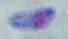
Summary:
  - Identification: Toxoplasma gondii
  - Magnification: 1000x
  - Modality: photomicrograph